Identify the parasite.
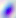
Toxoplasma gondii.

modality = micrograph
magnification = 400x